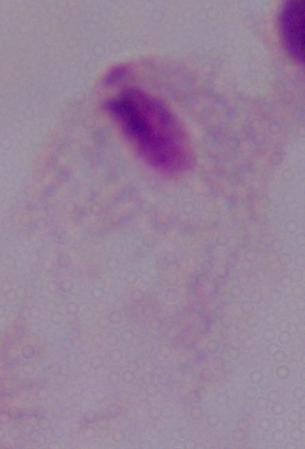

Summary:
  - Modality: micrograph
  - Magnification: 1000x
  - Identification: trichomonad